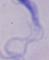
identification = trypanosome
modality = photomicrograph
magnification = 1000x